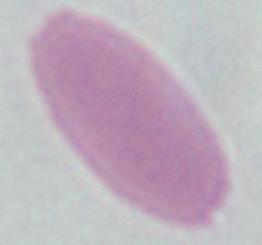

Photomicrograph. An erythrocyte is shown. Captured at 1000x magnification.